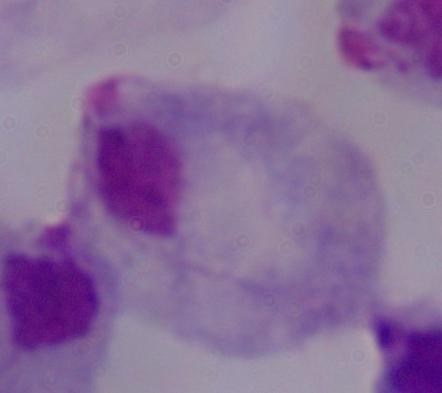

Summary:
  - Modality: photomicrograph
  - Magnification: 1000x
  - Identification: trichomonad